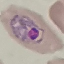

Summary:
  - Result: malaria parasites identified
  - Image type: cell patch, automatically extracted from a larger field of view and resized to 64 × 64 pixels
  - Preparation: thin smear
  - Stain: Giemsa
  - Capture: smartphone camera at the microscope eyepiece